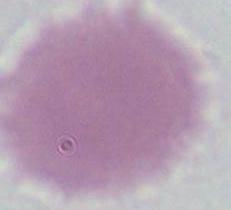

modality: micrograph
magnification: 1000x
identification: red blood cell